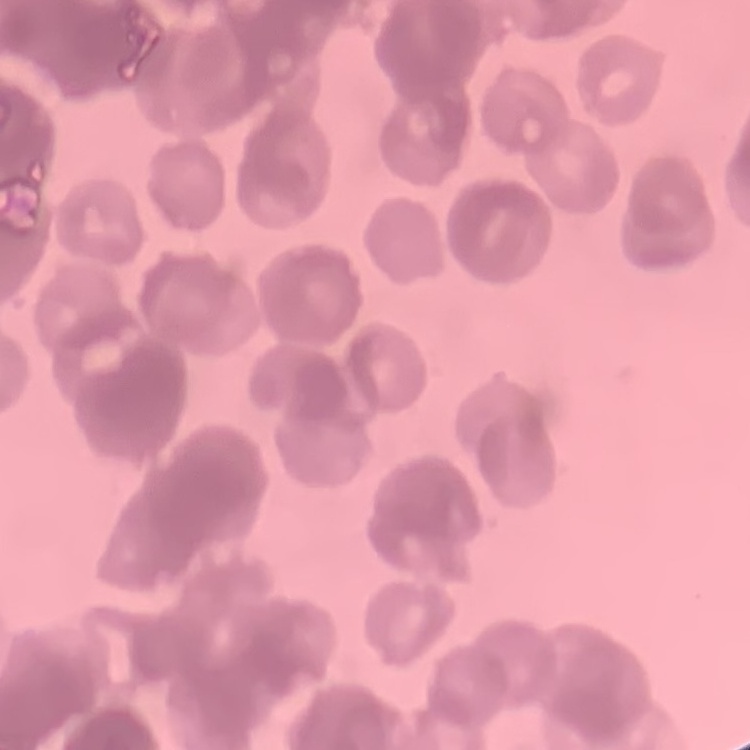 The erythrocytes show rouleaux formation. Thin blood smear. One tile cut from a larger photomicrograph. Field's or Giemsa stain.